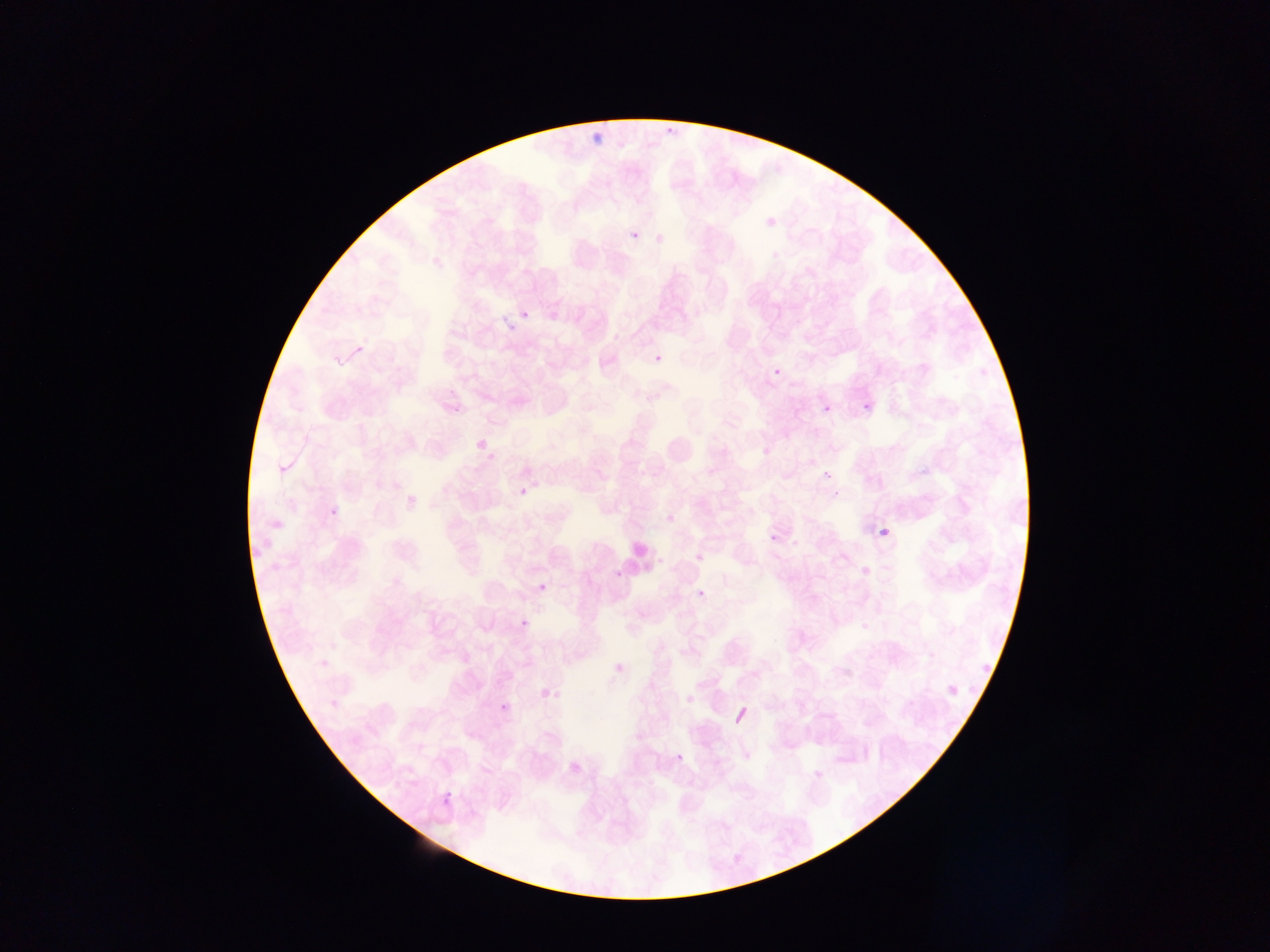
Approximate bounding boxes as (left, top, right, bottom) in pixels.
Summary:
  - Malaria parasite locations: (660, 114, 677, 136), (585, 130, 602, 148), (757, 210, 779, 227), (626, 227, 644, 245), (653, 234, 666, 246), (518, 301, 536, 325), (653, 348, 670, 366), (769, 362, 784, 387), (859, 397, 876, 411), (819, 405, 831, 414), (472, 414, 496, 448), (760, 449, 768, 459), (819, 465, 835, 479), (514, 479, 533, 501), (325, 499, 343, 517), (875, 524, 894, 548), (767, 532, 779, 555), (866, 566, 874, 576), (537, 581, 554, 597), (696, 590, 712, 602), (519, 610, 537, 636), (604, 660, 628, 684), (977, 661, 993, 670), (941, 674, 963, 700), (538, 684, 554, 710), (494, 689, 521, 719), (672, 754, 687, 767), (565, 757, 582, 777), (439, 788, 452, 806)
  - Leukocyte locations: (329, 335, 369, 374), (658, 428, 704, 476), (615, 539, 661, 580), (729, 704, 755, 730)
  - Preparation: thin blood smear
  - Capture: mobile-phone photograph through a microscope
  - Country: Ghana
  - Image size: 1270×952 pixels
  - Field of view: single